Name the blood parasite species.
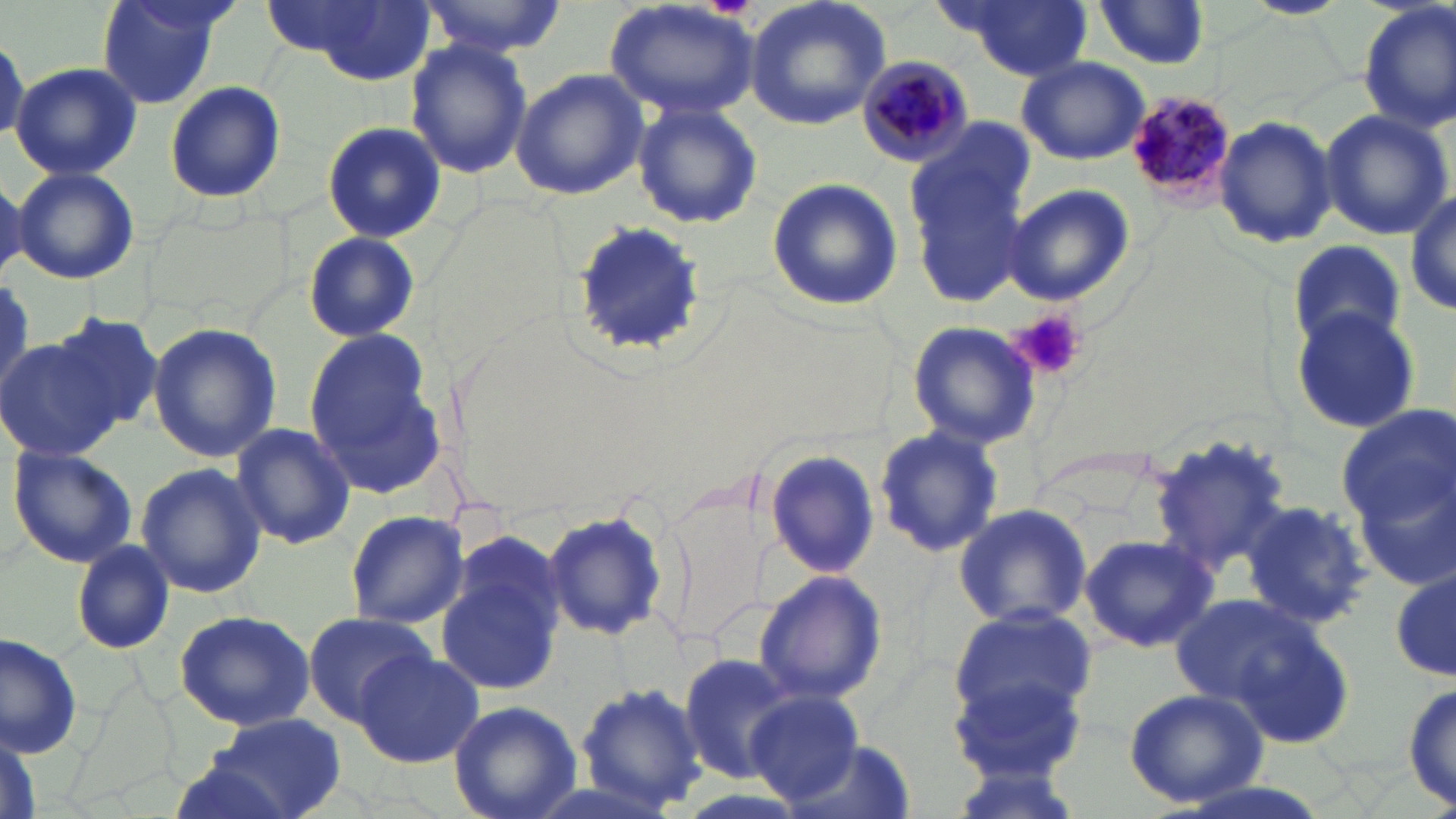
Plasmodium malariae.

Approximate bounding boxes as (x1, y1, x2, y2) in pixels. Platelet locations: (1014, 310, 1085, 380). Uninfected red blood cell locations: (96, 0, 228, 109), (418, 0, 566, 58), (605, 0, 760, 118), (744, 0, 891, 131), (940, 0, 1094, 79), (1245, 0, 1345, 18), (290, 1, 436, 82), (1094, 2, 1215, 71), (1356, 2, 1456, 135), (405, 40, 533, 179), (1017, 55, 1149, 165), (12, 61, 143, 179), (511, 67, 649, 201), (165, 81, 286, 205), (632, 102, 762, 230), (1318, 109, 1454, 241), (1210, 115, 1338, 249), (321, 120, 446, 243), (906, 130, 1034, 289), (12, 167, 140, 285), (0, 176, 28, 278), (766, 176, 904, 311), (1003, 183, 1135, 307), (1407, 189, 1456, 317), (572, 224, 704, 358), (303, 231, 418, 344), (1287, 240, 1406, 350), (1286, 306, 1420, 435), (45, 314, 165, 438), (907, 320, 1039, 449), (147, 322, 283, 462), (303, 329, 449, 495), (1, 336, 132, 460), (1341, 403, 1452, 573), (230, 421, 357, 549), (873, 429, 1002, 555), (1149, 434, 1296, 579), (9, 445, 138, 568), (763, 447, 880, 579), (136, 461, 267, 599), (1242, 501, 1372, 628), (953, 502, 1093, 630), (543, 508, 671, 642), (344, 509, 469, 630), (1080, 534, 1216, 653), (72, 540, 174, 654), (436, 554, 564, 697), (754, 569, 887, 705), (1391, 571, 1454, 684), (1169, 591, 1354, 746), (949, 606, 1097, 730), (174, 608, 316, 732), (300, 612, 438, 722), (0, 629, 85, 759), (352, 650, 483, 766), (946, 652, 1093, 783), (678, 653, 804, 782), (573, 680, 710, 814), (1404, 680, 1456, 813), (1122, 687, 1268, 809), (748, 691, 865, 805), (448, 700, 581, 819), (213, 713, 346, 819), (0, 724, 43, 819), (771, 735, 916, 819), (162, 754, 298, 819). Plasmodium malariae-infected red blood cell locations: (856, 55, 976, 170), (1128, 91, 1243, 208). Image is 1456×819 pixels. Light microscopy. 1000x magnification. Single field of view. May-Grünwald-Giemsa-stained preparation. Thin blood smear.